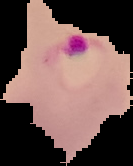

Image is 133×166 pixels. Malaria status: parasitized. The area outside the segmented cell region is set to black. From a thin blood smear.